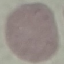

Summary:
  - Result: no malaria parasites detected
  - Stain: Giemsa
  - Preparation: thin blood smear
  - Image type: automatically extracted cell patch, resized to 64 × 64 pixels
  - Capture: smartphone camera at the microscope eyepiece